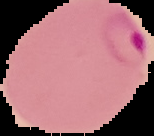

Segmented cell region on a black background. Image is 154×136 pixels. From a thin blood film. Malaria status: parasitized.